Give the position of every malaria parasite.
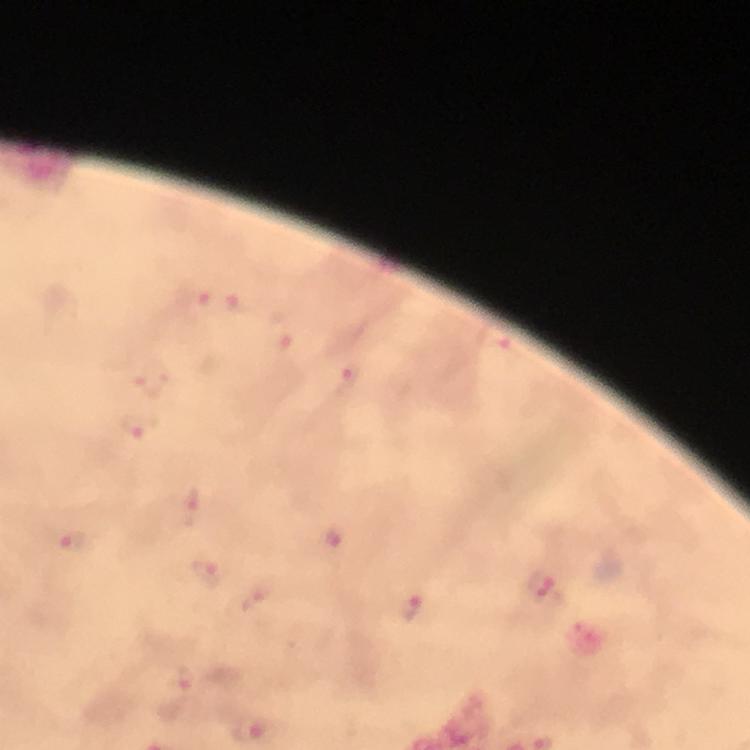

Approximate centers as [x, y] in pixels.
Malaria parasites: [197, 299], [239, 304], [281, 332], [347, 377], [141, 426], [189, 509], [331, 541], [71, 542], [207, 571], [541, 587], [257, 603], [413, 610], [176, 679], [257, 728].

Smartphone photograph taken through a microscope. Image is 750×750 pixels. Giemsa-stained preparation. From a malaria diagnostic workup. 100x magnification. Thick blood smear. Immersion oil applied. Cropped region of a single field of view.